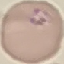
Summary:
  - Malaria status: parasitized
  - Capture: smartphone camera at the microscope eyepiece
  - Preparation: thin blood smear
  - Stain: Giemsa
  - Image type: cell patch, automatically extracted from a larger field of view and resized to 64 × 64 pixels